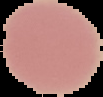

Summary:
  - Image size: 103×97 pixels
  - Malaria status: uninfected
  - Image type: cell region segmented out of the field of view; surrounding area masked to black
  - Preparation: thin blood smear